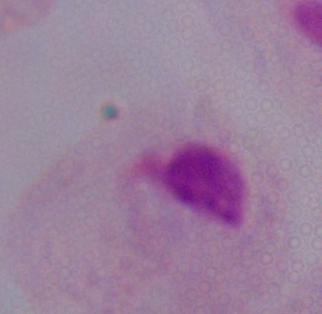
identification = trichomonad
magnification = 1000x
modality = micrograph